State which parasite is depicted.
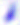
Toxoplasma gondii.

Summary:
  - Modality: photomicrograph
  - Magnification: 400x